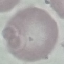
result = no malaria parasites seen
preparation = thin blood smear
capture = smartphone camera at the microscope eyepiece
stain = Giemsa
image type = automatically extracted cell patch, resized to 64 × 64 pixels